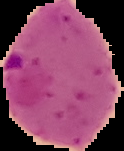
Image is 124×151 pixels. Result: Plasmodium parasites detected. The area outside the segmented cell region is set to black. From a thin blood film.